State which parasite is depicted.
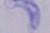

A trypanosome.

Micrograph. 1000x magnification.